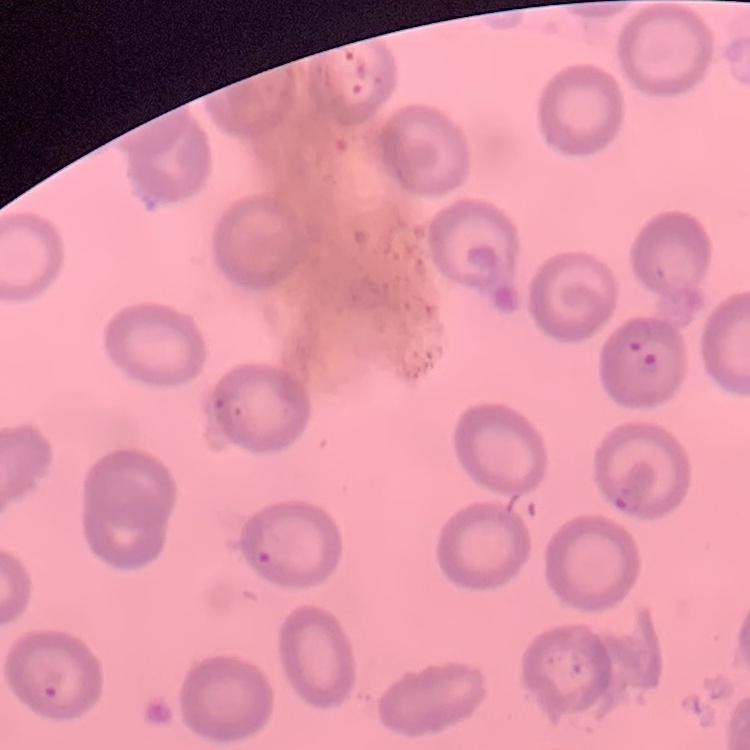
The red blood cells show no rouleaux formation. Thin peripheral smear. Square crop of a larger photomicrograph. Stained with either Field's or Giemsa.